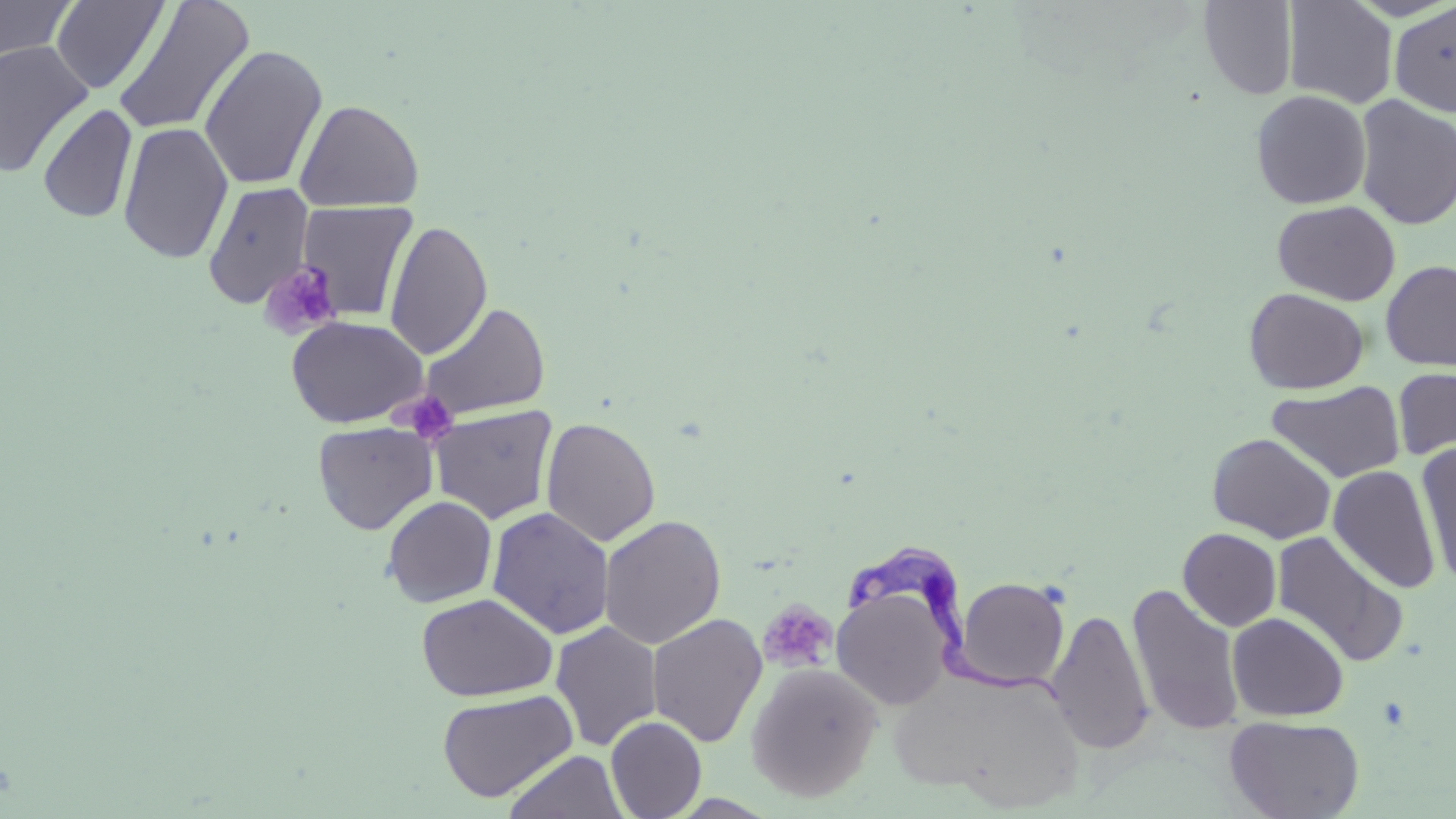 Approximate bounding boxes as [x1, y1, x2, y2] in pixels. Uninfected red blood cell locations: [0, 0, 77, 63], [1283, 0, 1397, 109], [50, 1, 169, 94], [112, 1, 255, 137], [1199, 1, 1297, 100], [1390, 2, 1456, 116], [0, 40, 94, 178], [199, 44, 327, 191], [1250, 89, 1372, 209], [1354, 95, 1456, 230], [294, 97, 425, 212], [37, 103, 138, 224], [117, 122, 233, 264], [201, 181, 314, 308], [1272, 199, 1400, 305], [296, 200, 418, 321], [384, 219, 493, 359], [1380, 260, 1456, 371], [1244, 288, 1368, 394], [419, 302, 550, 421], [287, 315, 428, 428], [1392, 367, 1456, 463], [1267, 380, 1406, 484], [430, 405, 557, 524], [541, 416, 661, 548], [312, 421, 438, 535], [1207, 433, 1336, 543], [1414, 443, 1456, 588], [1327, 465, 1440, 594], [381, 495, 497, 608], [487, 507, 614, 639], [599, 514, 726, 650], [1178, 528, 1281, 631], [1272, 530, 1407, 668], [954, 576, 1071, 690], [1127, 583, 1246, 737], [831, 584, 957, 712], [416, 593, 558, 702], [1047, 607, 1154, 755], [1227, 612, 1349, 722], [647, 613, 768, 748], [550, 620, 662, 752], [746, 662, 883, 802], [892, 667, 1086, 811], [437, 689, 578, 802], [1224, 715, 1364, 819], [605, 716, 706, 819], [503, 750, 628, 818]. Platelet locations: [256, 261, 343, 340], [395, 390, 457, 445], [757, 600, 837, 673]. Trypanosoma brucei locations: [846, 541, 1065, 710]. Slide-level diagnosis: Trypanosoma brucei. Image is 1456×819 pixels. Optical microscopy. May-Grünwald-Giemsa stain. Captured at 1000x magnification. Single field of view. Thin blood film.